State which parasite is depicted.
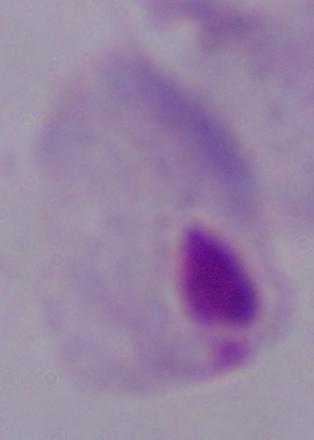
This is a trichomonad.

Summary:
  - Magnification: 1000x
  - Modality: photomicrograph